Point out each malaria parasite.
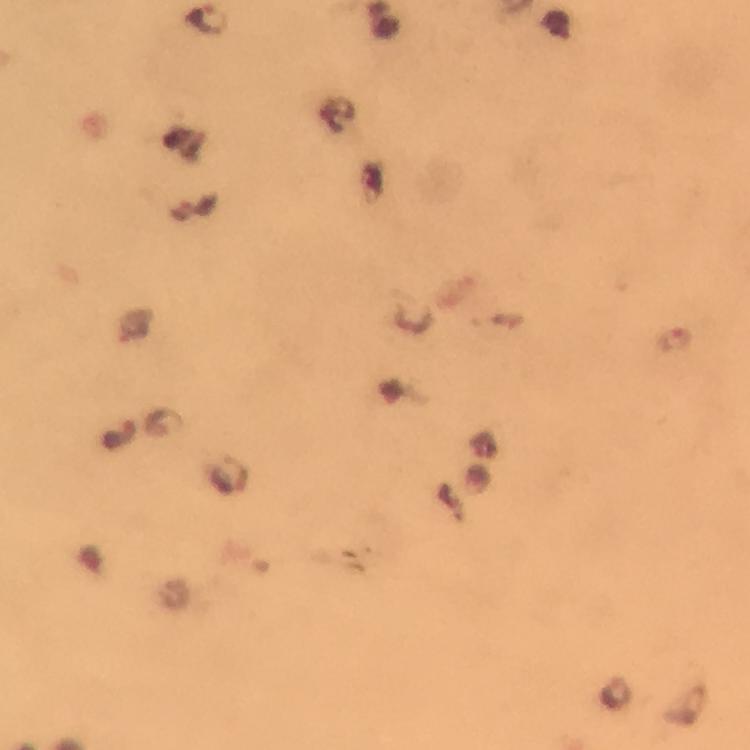

Approximate object centers, in pixels from the top-left corner.
Malaria parasites: (x=209, y=20), (x=676, y=340), (x=163, y=422), (x=116, y=434), (x=230, y=475), (x=617, y=693).

Summary:
  - Context: from a malaria diagnostic workup
  - Magnification: 100x
  - Image size: 750×750 pixels
  - Immersion oil: applied
  - Stain: Giemsa
  - Preparation: thick smear
  - Cropped from: one field of view
  - Capture: smartphone photograph through a microscope